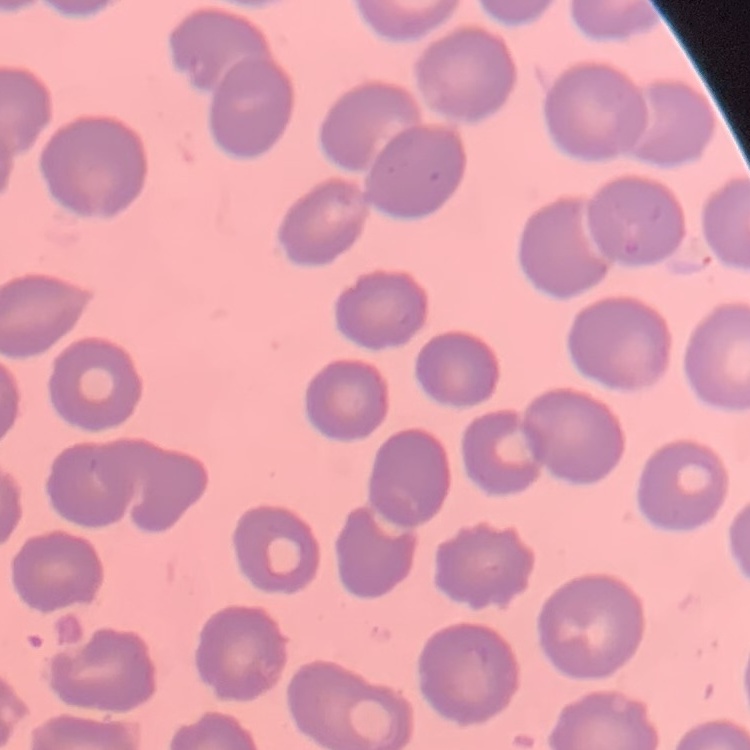

Summary:
  - Erythrocyte morphology: no rouleaux formation
  - Stain: Field's or Giemsa
  - Preparation: thin peripheral smear
  - Image type: one tile cut from a larger photomicrograph